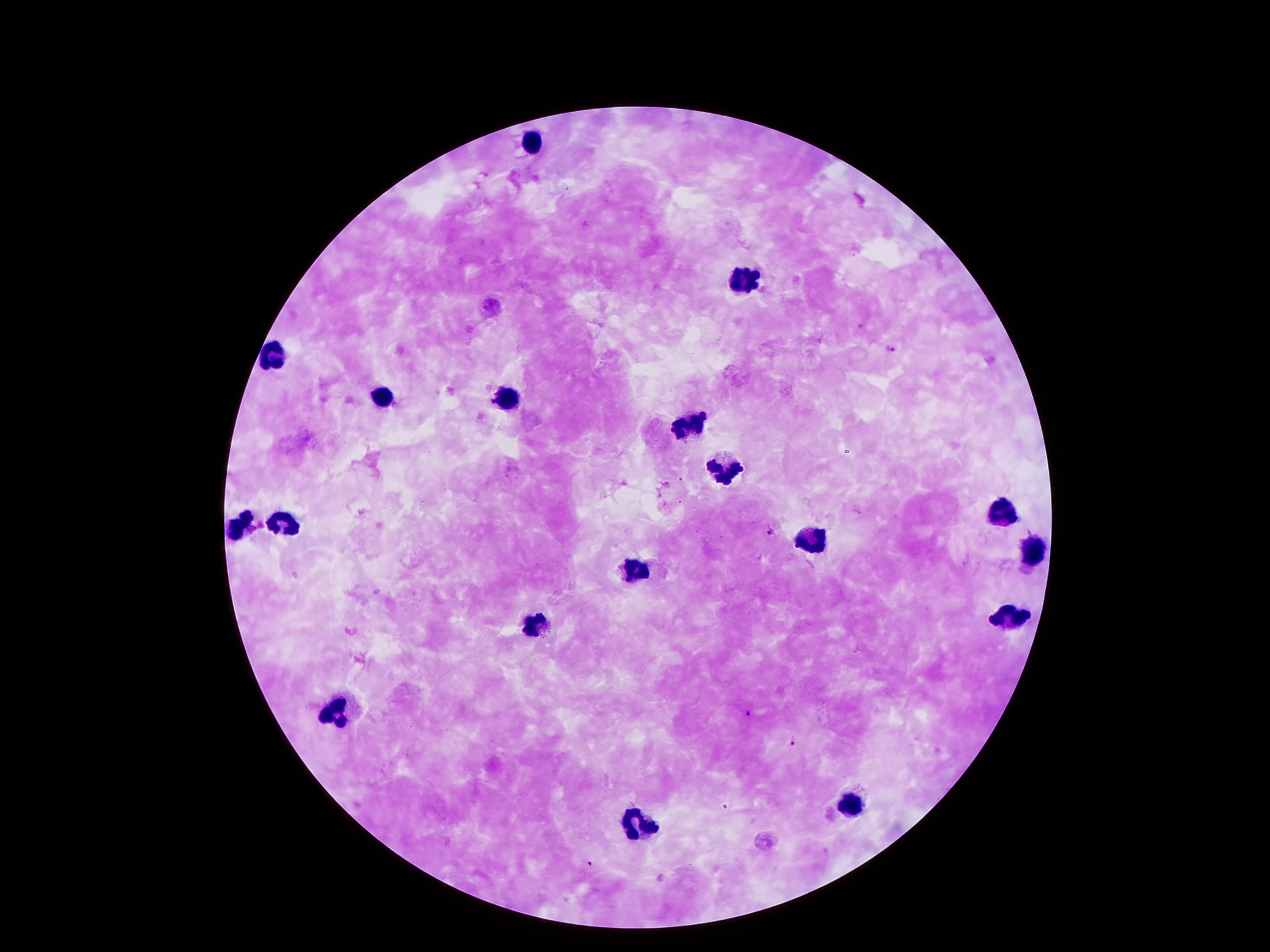

coordinate format = approximate centers as (x, y) in pixels
leukocyte locations = (533, 142), (743, 282), (267, 356), (385, 394), (511, 400), (687, 426), (725, 472), (1003, 510), (291, 522), (239, 528), (809, 542), (1033, 550), (635, 570), (1013, 618), (533, 625), (333, 708), (851, 804), (641, 822)
Plasmodium parasite locations = (891, 349), (770, 531), (749, 711), (795, 741), (591, 865)
patient malaria status = positive for Plasmodium falciparum
magnification = 100x
field of view = single
preparation = thick peripheral-blood smear
capture = smartphone through the microscope eyepiece
image size = 1270×952 pixels
stain = Giemsa